Give the preparation type.
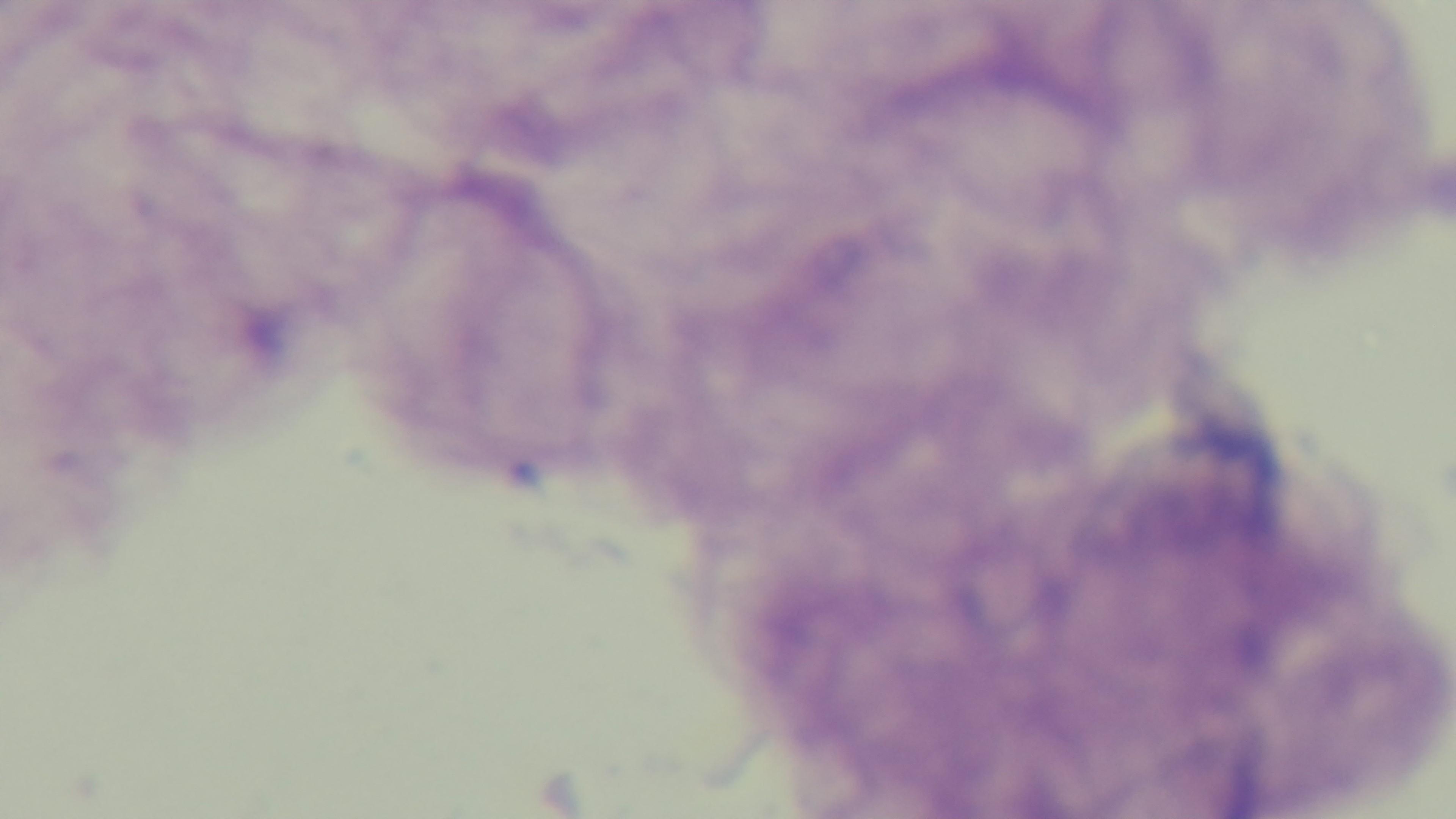
A thick smear.

capture = mounted 4K digital camera
modality = light microscopy
stain = Giemsa
objective = 100x oil immersion
field of view = one from the slide
malaria status = uninfected